Name the parasite shown.
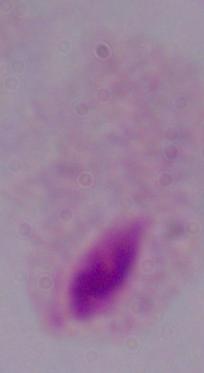

A trichomonad.

1000x magnification. Photomicrograph.